Outline each blood parasite and name the species.
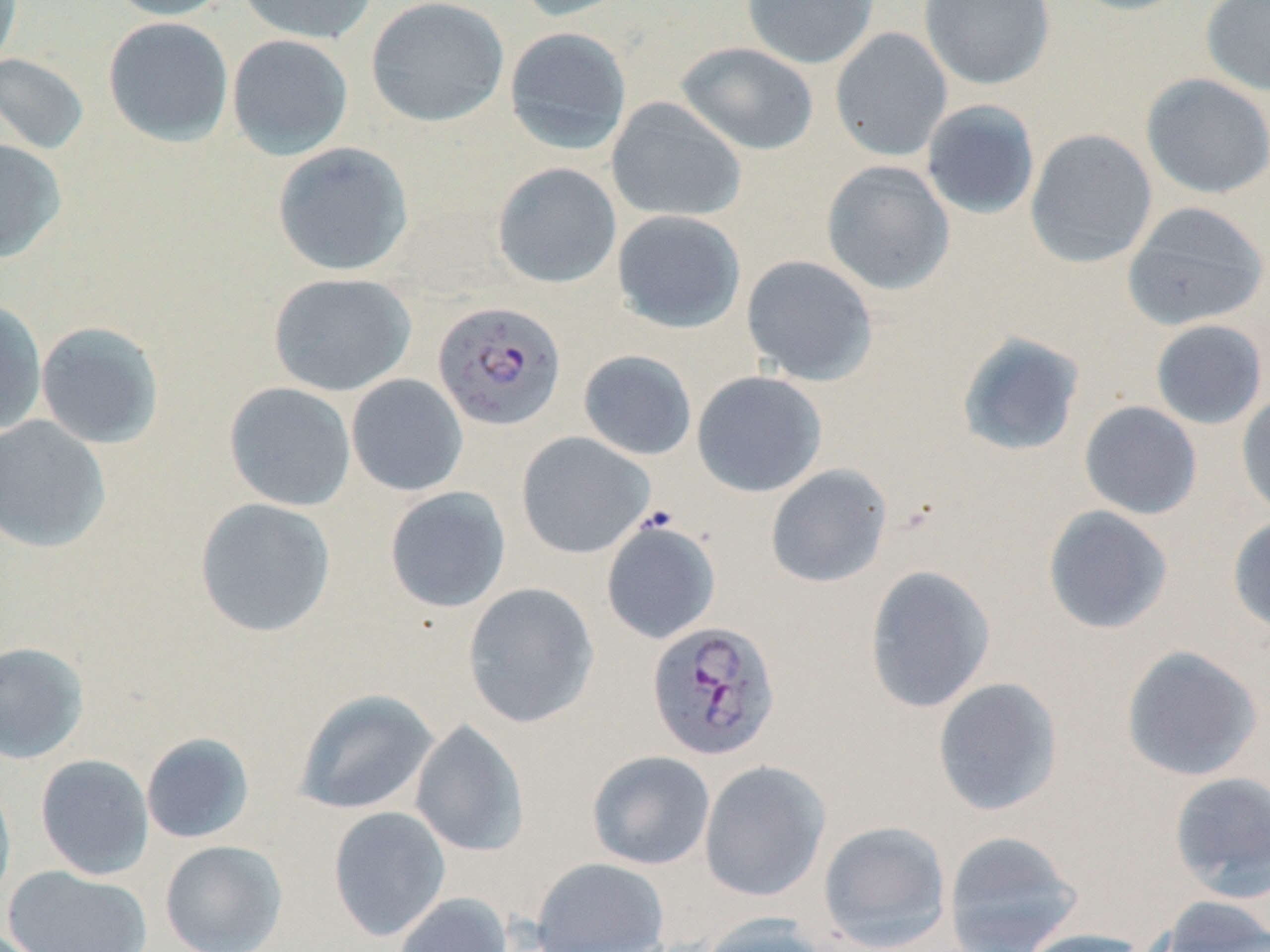

Approximate bounding boxes as [x1, y1, x2, y2] in pixels.
Plasmodium falciparum-infected red blood cells: [433, 300, 567, 430], [646, 621, 781, 762].
No Plasmodium ovale, Plasmodium malariae, Plasmodium vivax, Babesia divergens, or Trypanosoma brucei observed.

Uninfected red blood cell locations: [0, 0, 23, 71], [104, 0, 232, 20], [236, 0, 376, 44], [366, 0, 509, 127], [510, 0, 639, 22], [741, 0, 879, 70], [918, 0, 1055, 90], [1064, 0, 1196, 16], [1200, 0, 1270, 97], [102, 16, 234, 148], [504, 26, 633, 155], [830, 27, 953, 161], [226, 34, 354, 160], [676, 41, 819, 156], [0, 53, 90, 155], [1140, 73, 1270, 200], [606, 97, 747, 222], [920, 100, 1040, 220], [1025, 129, 1158, 268], [0, 138, 67, 264], [272, 141, 414, 277], [821, 160, 955, 295], [492, 162, 622, 288], [1122, 201, 1270, 331], [611, 209, 747, 334], [741, 255, 879, 386], [267, 272, 417, 396], [0, 299, 47, 435], [1150, 319, 1268, 429], [35, 321, 165, 449], [956, 332, 1085, 457], [578, 350, 697, 460], [692, 371, 827, 497], [346, 374, 468, 497], [224, 382, 356, 511], [1236, 390, 1270, 520], [1078, 400, 1203, 520], [0, 415, 112, 554], [516, 432, 654, 559], [765, 464, 892, 588], [384, 487, 511, 613], [194, 497, 336, 638], [1042, 505, 1174, 635], [1227, 514, 1270, 634], [601, 519, 721, 644], [864, 565, 995, 713], [462, 582, 599, 728], [0, 641, 89, 764], [1120, 644, 1264, 782], [932, 677, 1064, 816], [294, 688, 439, 815], [410, 720, 529, 857], [141, 733, 255, 844], [587, 750, 715, 870], [35, 754, 154, 880], [699, 760, 831, 901], [1168, 771, 1270, 900], [0, 774, 16, 910], [328, 806, 450, 941], [818, 820, 952, 951], [942, 830, 1083, 952], [160, 840, 287, 952], [531, 857, 670, 951], [4, 865, 152, 952], [393, 892, 513, 952], [1151, 896, 1270, 952], [697, 913, 830, 952], [1016, 928, 1154, 952]. Slide-level diagnosis: Plasmodium falciparum. Captured at 1000x magnification. Thin blood film. Image is 1270×952 pixels. Light microscopy. May-Grünwald-Giemsa stain. Single field of view.